Describe the morphology of the red blood cells.
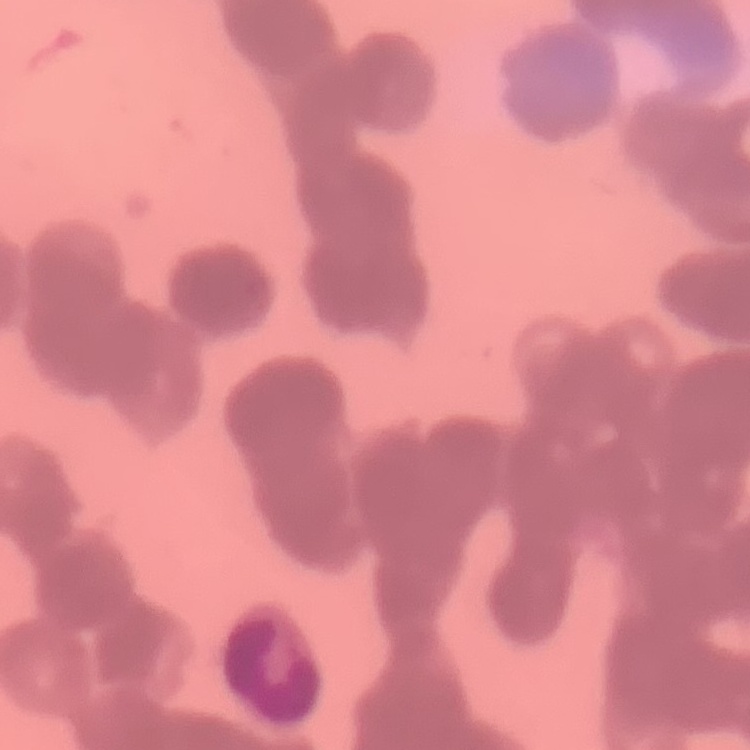
Rouleaux formation.

One tile cut from a larger photomicrograph. Thin peripheral smear. Stained with either Field's or Giemsa.